Locate every blood parasite and identify its species.
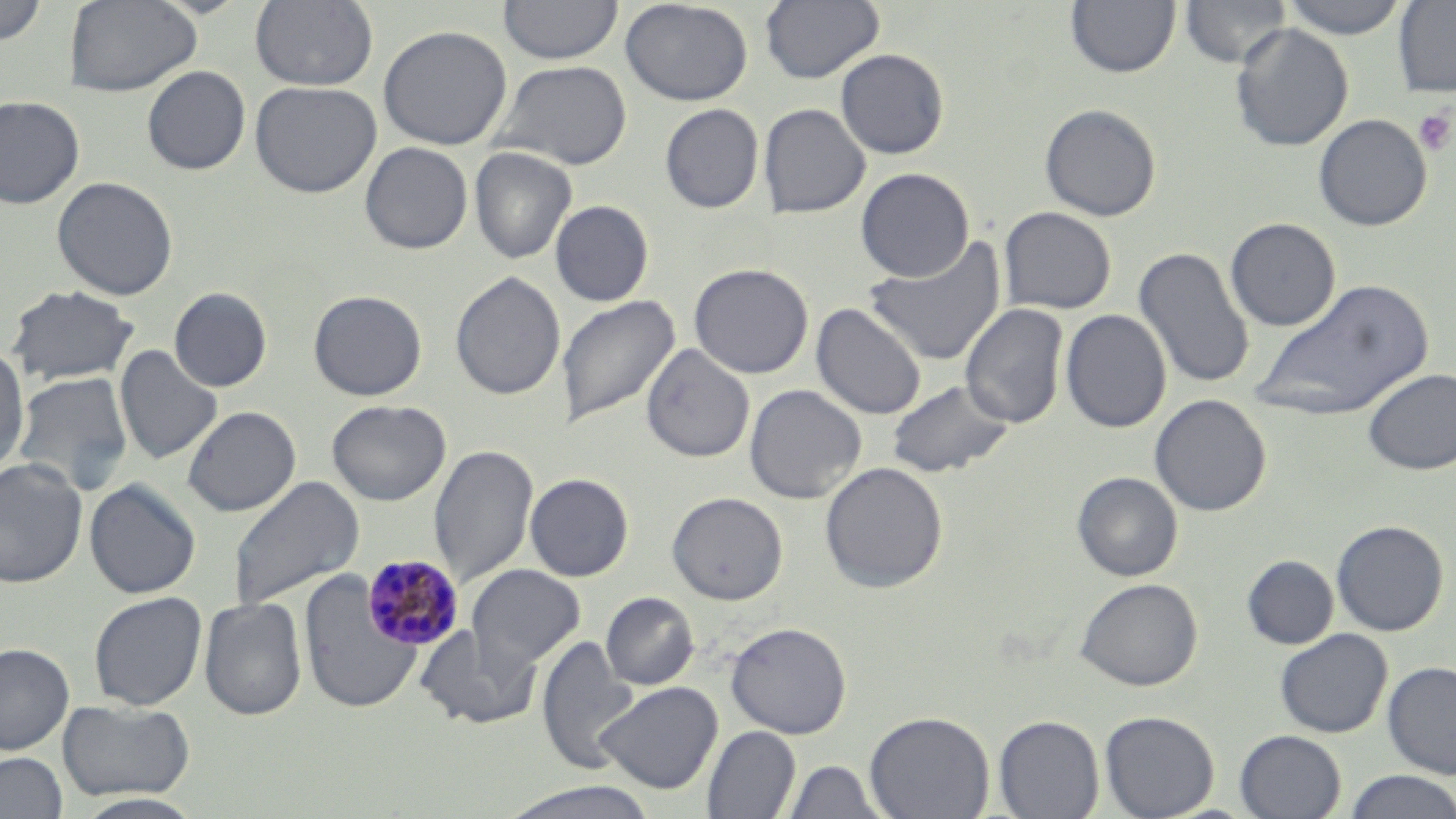
Approximate bounding boxes as named x1/y1/x2/y2 corners in pixels.
Plasmodium malariae-infected red blood cells: (x1=362, y1=554, x2=464, y2=650).
No Plasmodium falciparum, Plasmodium ovale, Plasmodium vivax, Babesia divergens, or Trypanosoma brucei observed.

slide-level diagnosis = Plasmodium malariae
magnification = 1000x
preparation = thin blood smear
platelet locations = approximate bounding boxes as named x1/y1/x2/y2 corners in pixels: (x1=1413, y1=108, x2=1455, y2=156)
modality = optical microscopy
stain = May-Grünwald-Giemsa
uninfected red blood cell locations = approximate bounding boxes as named x1/y1/x2/y2 corners in pixels: (x1=64, y1=0, x2=201, y2=97), (x1=250, y1=0, x2=379, y2=91), (x1=498, y1=0, x2=623, y2=64), (x1=620, y1=0, x2=753, y2=106), (x1=760, y1=0, x2=884, y2=84), (x1=1180, y1=0, x2=1292, y2=68), (x1=1277, y1=0, x2=1412, y2=38), (x1=1393, y1=0, x2=1456, y2=98), (x1=0, y1=1, x2=49, y2=45), (x1=1066, y1=1, x2=1180, y2=78), (x1=1230, y1=23, x2=1353, y2=151), (x1=378, y1=24, x2=512, y2=150), (x1=835, y1=48, x2=949, y2=159), (x1=491, y1=60, x2=633, y2=170), (x1=142, y1=66, x2=251, y2=175), (x1=250, y1=81, x2=381, y2=197), (x1=0, y1=95, x2=85, y2=209), (x1=659, y1=103, x2=764, y2=213), (x1=759, y1=103, x2=870, y2=218), (x1=1039, y1=103, x2=1161, y2=221), (x1=1313, y1=113, x2=1432, y2=231), (x1=359, y1=142, x2=473, y2=254), (x1=469, y1=146, x2=577, y2=264), (x1=855, y1=167, x2=974, y2=282), (x1=52, y1=176, x2=178, y2=300), (x1=550, y1=200, x2=654, y2=306), (x1=999, y1=206, x2=1117, y2=314), (x1=1224, y1=217, x2=1341, y2=332), (x1=864, y1=238, x2=1007, y2=366), (x1=1132, y1=246, x2=1255, y2=389), (x1=689, y1=263, x2=814, y2=379), (x1=450, y1=271, x2=566, y2=400), (x1=1250, y1=278, x2=1433, y2=423), (x1=5, y1=285, x2=141, y2=386), (x1=169, y1=287, x2=272, y2=392), (x1=308, y1=289, x2=427, y2=401), (x1=557, y1=294, x2=680, y2=427), (x1=811, y1=303, x2=926, y2=419), (x1=960, y1=303, x2=1068, y2=429), (x1=1060, y1=309, x2=1172, y2=433), (x1=641, y1=343, x2=754, y2=463), (x1=114, y1=345, x2=223, y2=464), (x1=0, y1=346, x2=30, y2=476), (x1=1362, y1=368, x2=1456, y2=475), (x1=11, y1=371, x2=134, y2=495), (x1=886, y1=378, x2=1014, y2=479), (x1=744, y1=383, x2=867, y2=504), (x1=1149, y1=394, x2=1271, y2=517), (x1=326, y1=399, x2=451, y2=505), (x1=182, y1=406, x2=300, y2=516), (x1=429, y1=443, x2=539, y2=588), (x1=0, y1=458, x2=88, y2=589), (x1=820, y1=461, x2=948, y2=593), (x1=1072, y1=471, x2=1183, y2=581), (x1=525, y1=473, x2=634, y2=581), (x1=227, y1=475, x2=365, y2=612), (x1=84, y1=479, x2=201, y2=598), (x1=667, y1=492, x2=788, y2=605), (x1=1331, y1=519, x2=1449, y2=636), (x1=1242, y1=555, x2=1339, y2=649), (x1=466, y1=564, x2=585, y2=672), (x1=299, y1=569, x2=421, y2=714), (x1=1075, y1=577, x2=1203, y2=691), (x1=88, y1=591, x2=207, y2=711), (x1=600, y1=592, x2=699, y2=690), (x1=199, y1=596, x2=307, y2=720), (x1=725, y1=621, x2=851, y2=738), (x1=415, y1=624, x2=539, y2=730), (x1=1275, y1=628, x2=1392, y2=737), (x1=537, y1=635, x2=640, y2=774), (x1=0, y1=642, x2=75, y2=755), (x1=1382, y1=661, x2=1456, y2=779), (x1=596, y1=681, x2=722, y2=794), (x1=57, y1=699, x2=195, y2=801), (x1=864, y1=710, x2=994, y2=819), (x1=1099, y1=710, x2=1219, y2=819), (x1=994, y1=714, x2=1104, y2=818), (x1=702, y1=725, x2=800, y2=818), (x1=1235, y1=729, x2=1346, y2=819), (x1=0, y1=752, x2=68, y2=818), (x1=783, y1=760, x2=884, y2=817), (x1=1342, y1=771, x2=1456, y2=818), (x1=499, y1=781, x2=659, y2=819), (x1=75, y1=793, x2=206, y2=818)
image size = 1456×819 pixels
field of view = one of a larger specimen